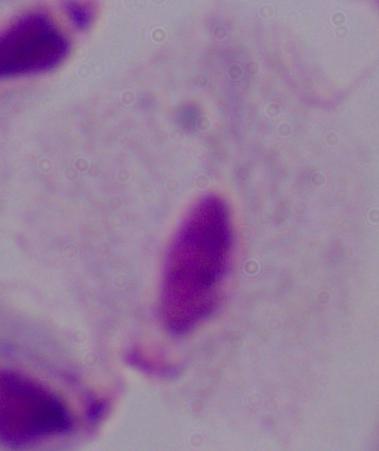

Summary:
  - Modality: photomicrograph
  - Identification: trichomonad
  - Magnification: 1000x